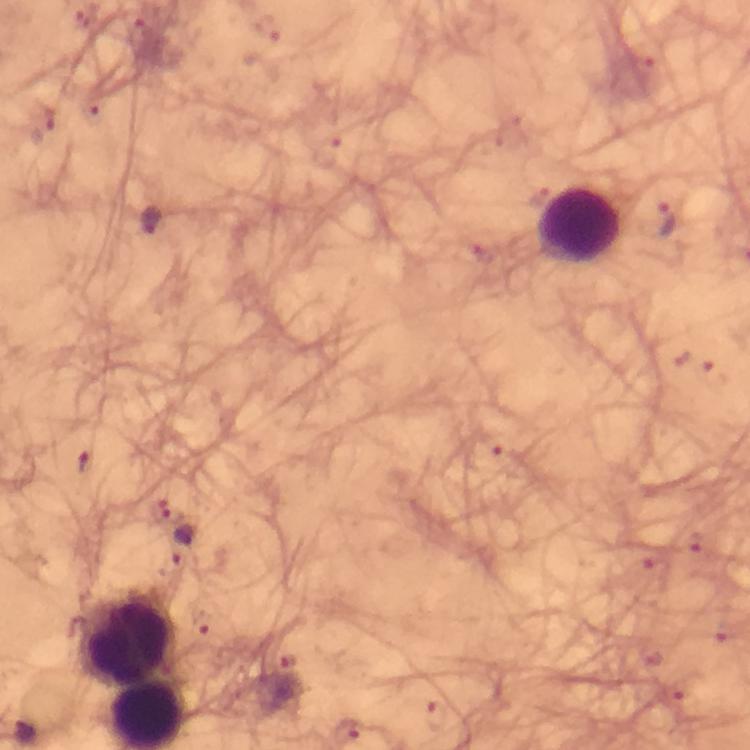

Approximate centers as {x, y} in pixels.
Summary:
  - Leukocyte locations: {580, 224}, {126, 639}
  - Plasmodium parasite locations: {151, 219}, {665, 219}, {185, 544}, {25, 731}
  - Magnification: 100x
  - Cropped from: one field of view
  - Preparation: thick blood smear
  - Image size: 750×750 pixels
  - Context: from a malaria diagnostic workup
  - Immersion oil: applied
  - Stain: Giemsa
  - Capture: smartphone photograph through a microscope